Comment on the morphology of the erythrocytes.
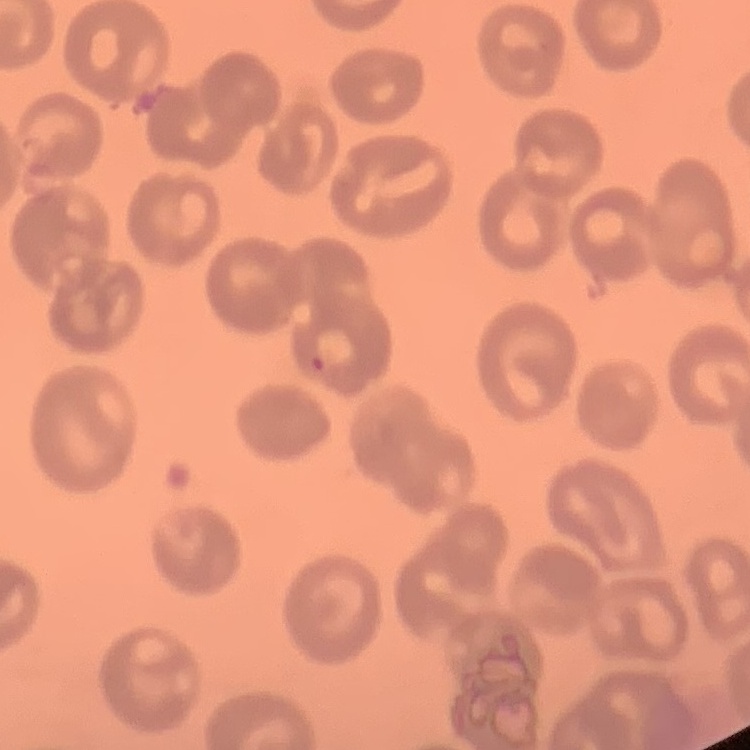
No rouleaux formation.

Thin peripheral smear. One tile cut from a larger photomicrograph. Field's or Giemsa stain.